Name the blood parasite species.
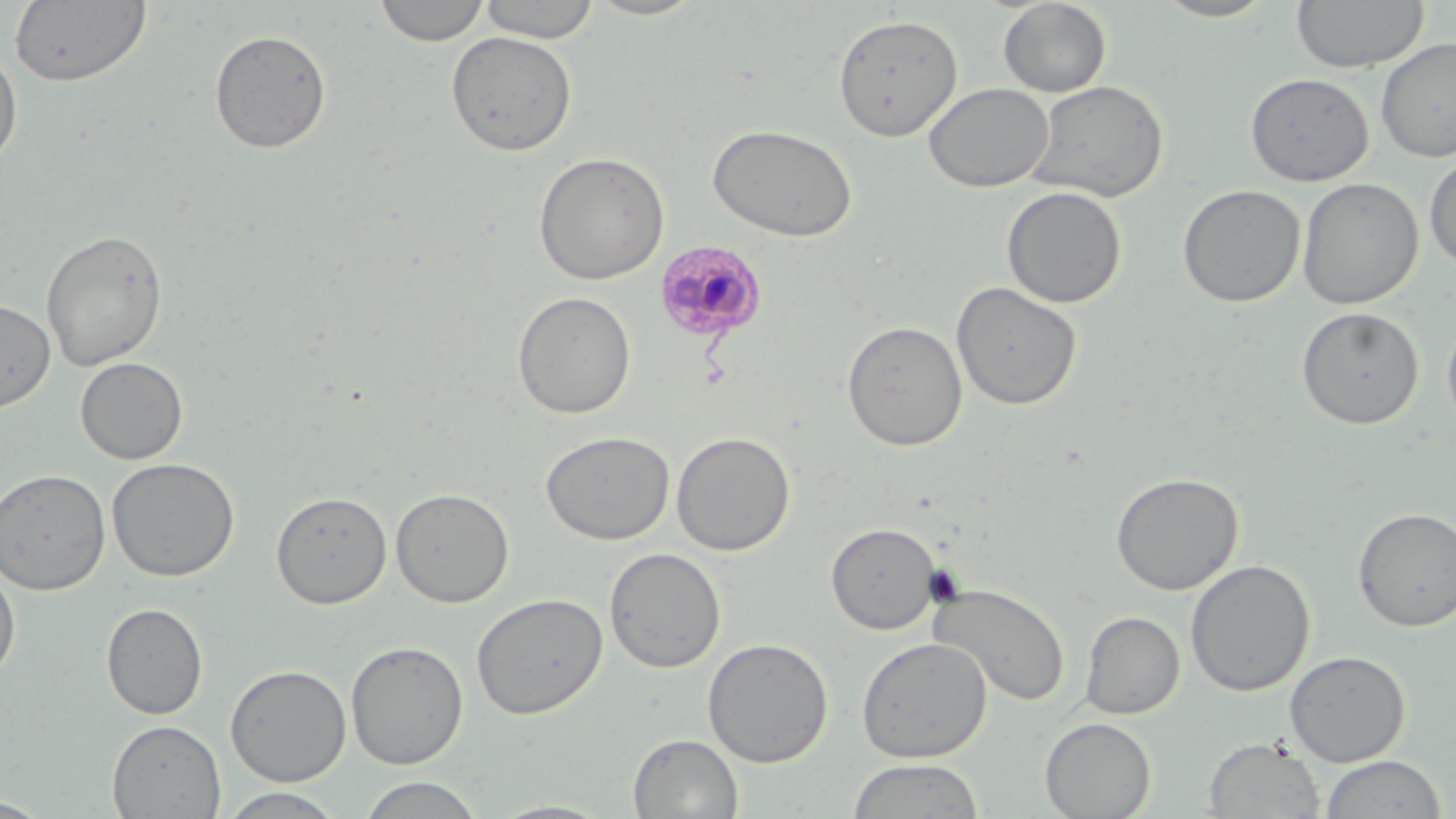

Plasmodium malariae.

{
  "stain": "May-Grünwald-Giemsa",
  "magnification": "1000x",
  "plasmodium_malariae_infected_red_blood_cell_locations": "approximate bounding boxes as (x1,y1)-(x2,y2) corner pairs in pixels: (653,239)-(769,344)",
  "modality": "light microscopy",
  "preparation": "thin blood film",
  "field_of_view": "one of a larger specimen",
  "uninfected_red_blood_cell_locations": "approximate bounding boxes as (x1,y1)-(x2,y2) corner pairs in pixels: (374,0)-(490,47), (583,0)-(707,21), (1150,0)-(1281,22), (9,1)-(152,88), (478,1)-(600,43), (997,1)-(1112,97), (1291,1)-(1429,73), (833,13)-(963,143), (209,28)-(332,153), (445,30)-(578,157), (1376,38)-(1456,162), (0,46)-(23,170), (1244,72)-(1374,186), (1027,79)-(1169,203), (923,82)-(1054,193), (707,123)-(858,242), (533,151)-(670,285), (1423,151)-(1456,274), (1296,177)-(1424,310), (1177,184)-(1305,308), (1001,186)-(1127,309), (41,229)-(167,371), (950,280)-(1083,411), (513,291)-(636,419), (0,299)-(56,411), (1296,306)-(1424,429), (1441,306)-(1456,437), (842,320)-(968,452), (75,357)-(188,465), (540,430)-(675,545), (671,431)-(796,556), (106,457)-(240,581), (0,468)-(111,595), (1110,471)-(1244,596), (390,487)-(514,608), (271,490)-(392,609), (1352,507)-(1456,632), (826,522)-(940,635), (604,547)-(726,673), (1185,559)-(1314,697), (0,564)-(21,683), (929,582)-(1071,706), (471,592)-(608,720), (101,602)-(208,720), (1080,611)-(1185,719), (856,636)-(992,762), (702,637)-(834,768), (345,640)-(468,769), (1285,650)-(1410,766), (225,664)-(352,786), (1039,717)-(1156,818), (107,719)-(226,818), (628,733)-(743,818), (1203,737)-(1325,818), (1319,755)-(1447,818), (845,758)-(986,818), (356,776)-(487,818), (216,788)-(347,818), (0,796)-(53,817), (486,800)-(617,818)",
  "image_size": "1456×819 pixels"
}